State which parasite is depicted.
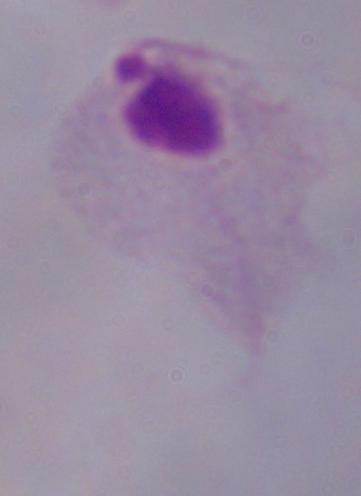

This is a trichomonad.

Micrograph. Captured at 1000x magnification.